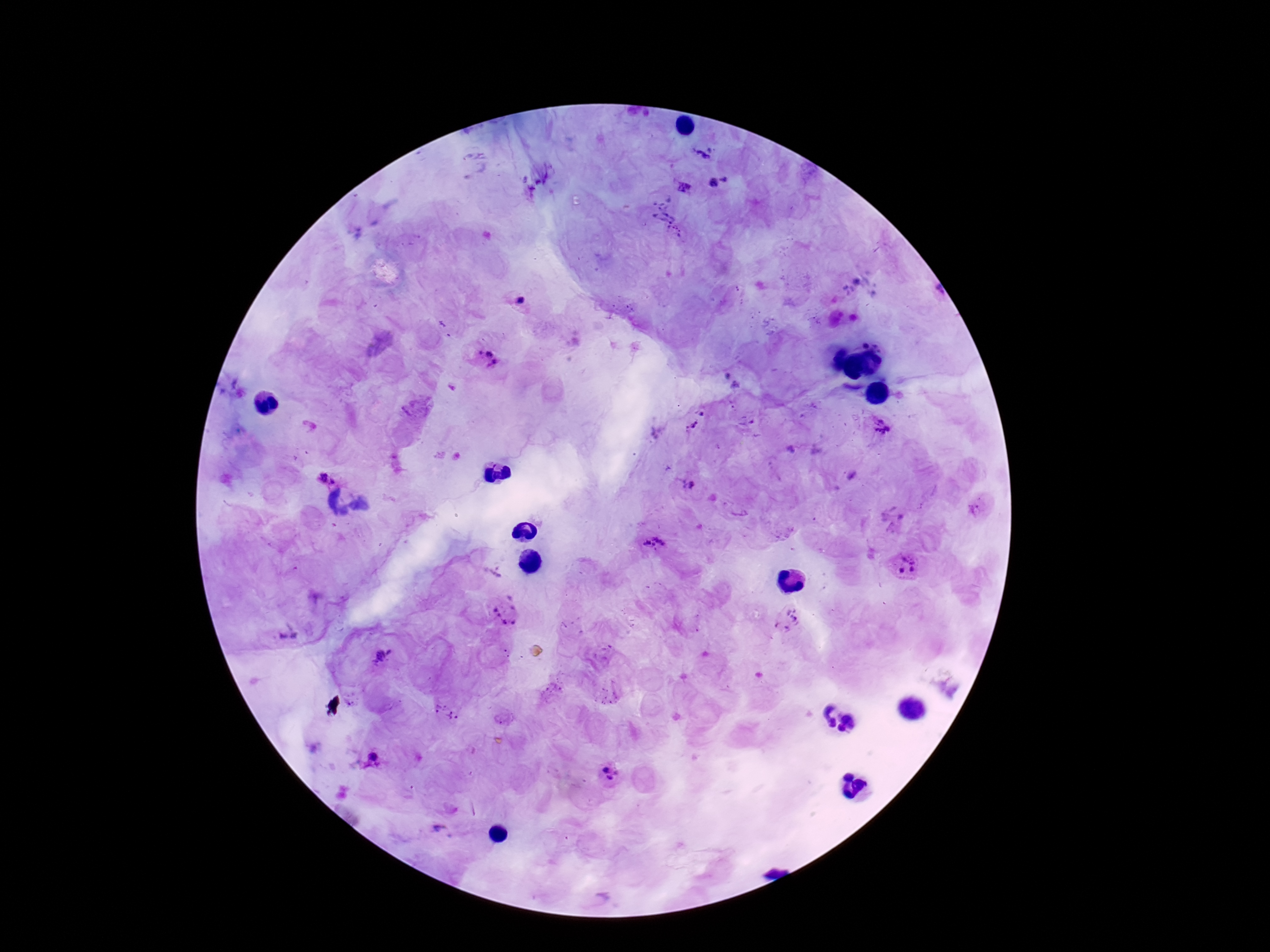
capture = smartphone camera through the microscope eyepiece
Plasmodium parasite locations = approximate object centers, in pixels from the top-left corner: (x=705, y=151), (x=721, y=184), (x=684, y=186), (x=679, y=233), (x=519, y=297), (x=485, y=357), (x=703, y=411), (x=691, y=427), (x=879, y=429), (x=324, y=471), (x=689, y=485), (x=652, y=544), (x=904, y=566), (x=506, y=611), (x=790, y=619), (x=287, y=635), (x=382, y=655), (x=444, y=713), (x=374, y=756), (x=611, y=774), (x=443, y=830)
stain = Giemsa
preparation = thick blood film
magnification = 100x
field of view = one from this slide
patient malaria status = infected
image size = 1270×952 pixels